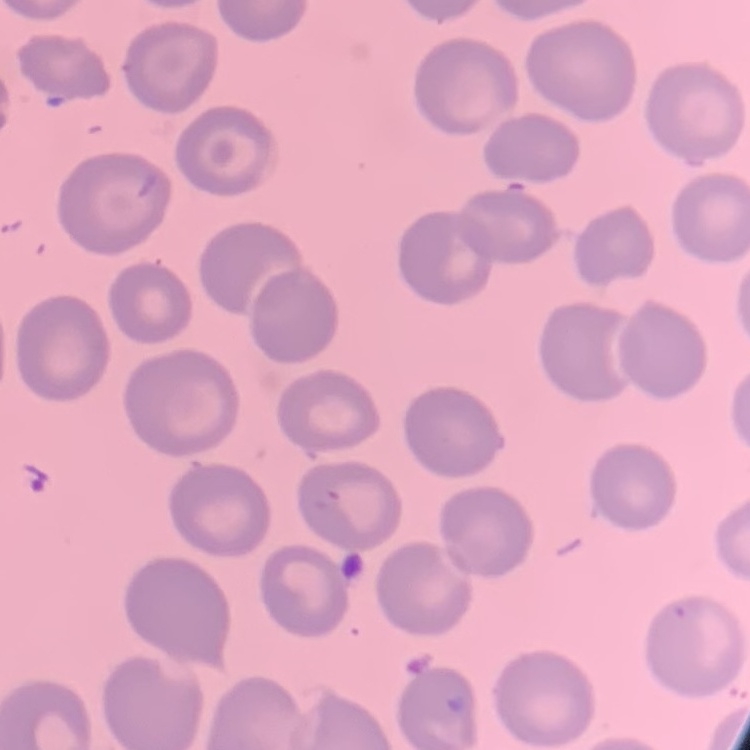 The erythrocytes show no rouleaux formation. Thin blood film. One tile cut from a larger photomicrograph. Stained with either Field's or Giemsa.